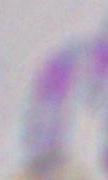

Summary:
  - Identification: Toxoplasma gondii
  - Magnification: 1000x
  - Modality: micrograph